Point out each malaria parasite and each leukocyte.
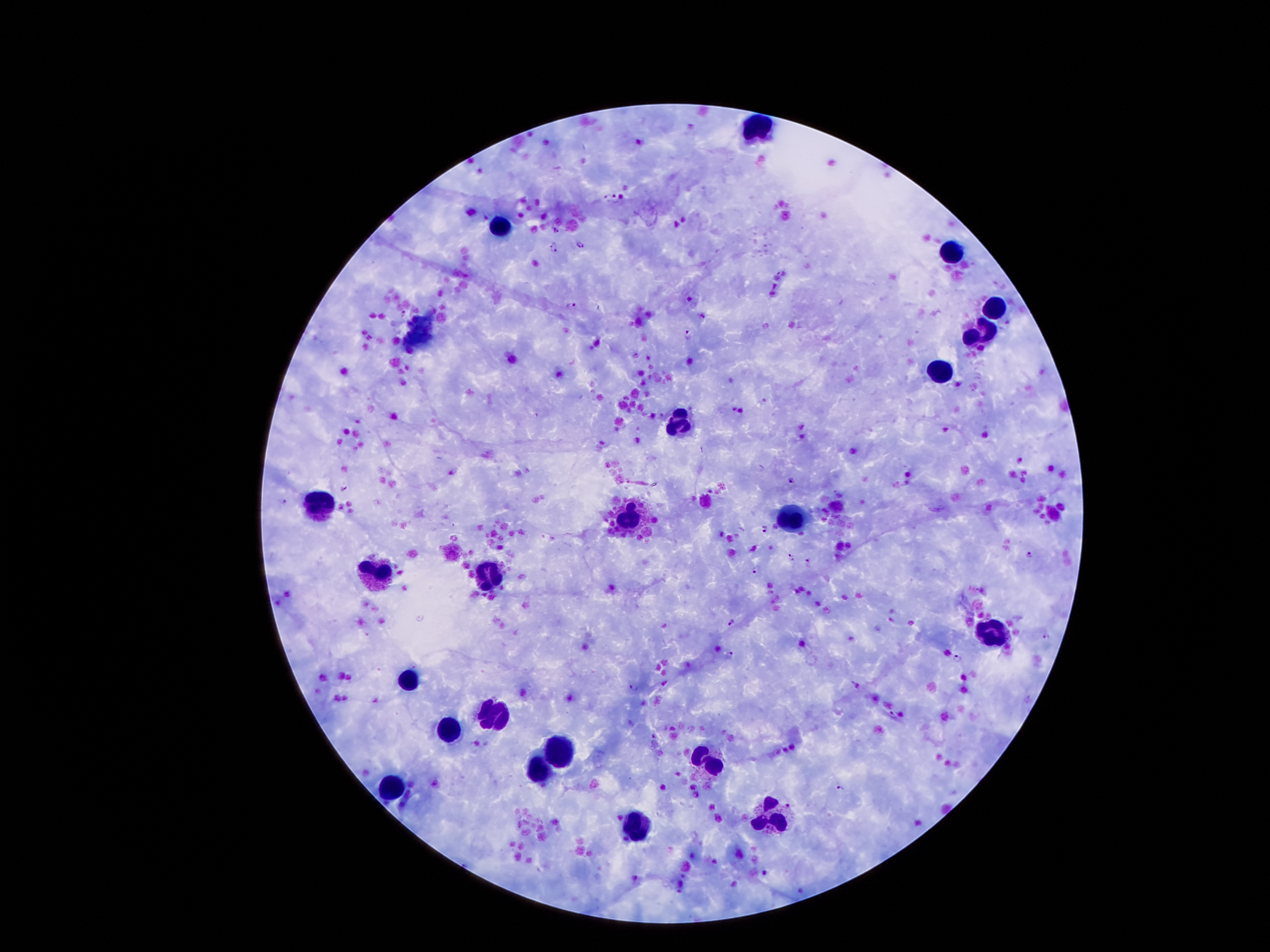
Approximate centers as [x, y] in pixels.
Malaria parasites: [605, 198], [615, 198], [555, 230], [580, 244], [554, 248], [572, 306], [403, 314], [688, 334], [792, 481], [344, 487], [282, 501], [764, 528], [1029, 556], [791, 558], [808, 560], [756, 569], [732, 622], [1047, 638], [728, 654], [957, 658], [634, 687], [893, 715], [839, 788].
Leukocytes: [754, 129], [502, 226], [954, 249], [995, 308], [985, 332], [940, 374], [673, 422], [317, 505], [631, 517], [797, 518], [377, 570], [489, 572], [993, 634], [408, 682], [492, 717], [447, 731], [558, 753], [712, 765], [538, 771], [390, 790], [774, 817], [633, 833].

Summary:
  - Magnification: 100x
  - Capture: smartphone camera through the microscope eyepiece
  - Preparation: thick blood film
  - Stain: Giemsa
  - Patient malaria status: infected with Plasmodium falciparum
  - Field of view: single
  - Image size: 1270×952 pixels